Locate and identify every blood parasite.
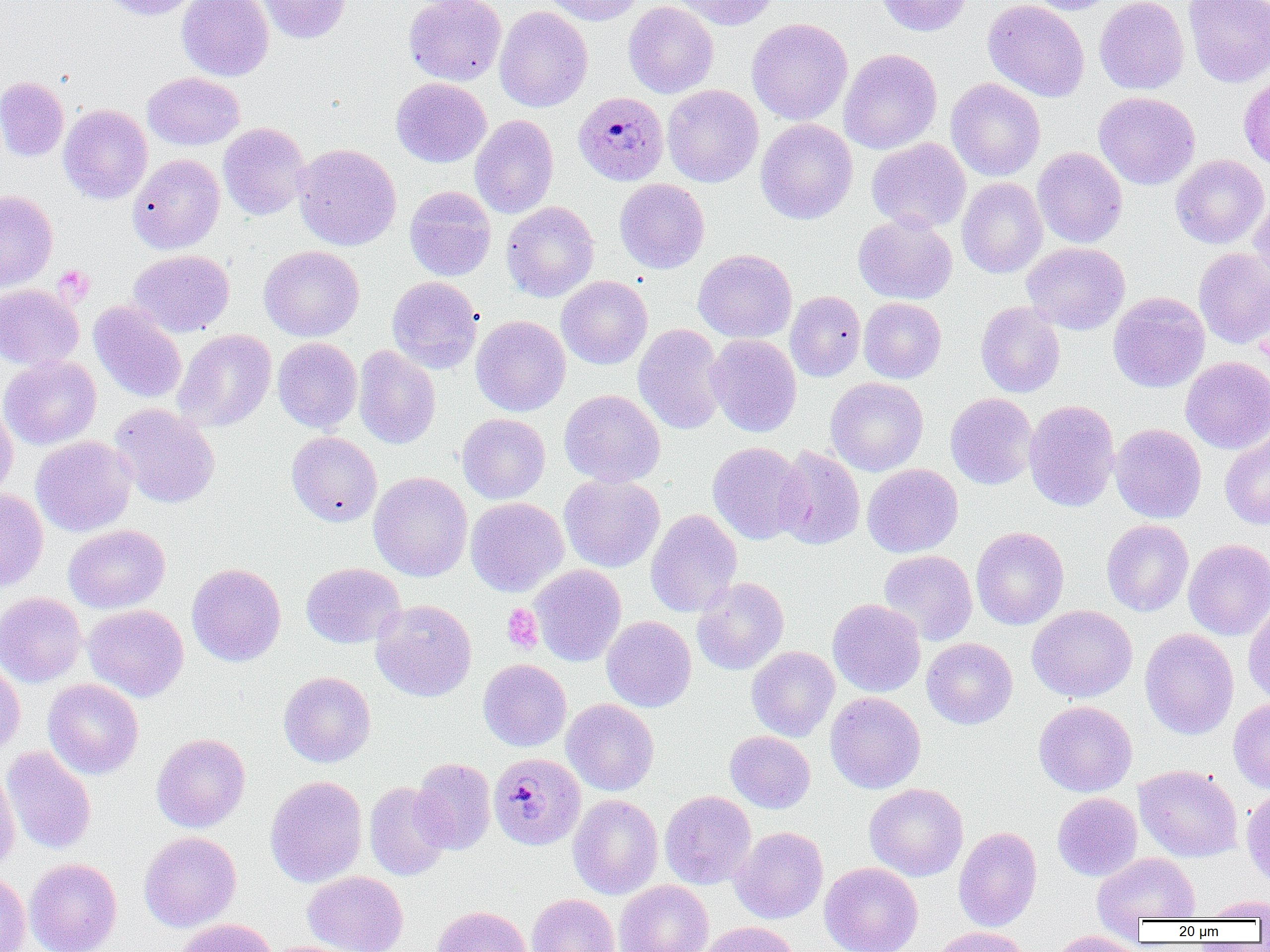

Approximate bounding boxes as named x1/y1/x2/y2 corners in pixels.
Plasmodium malariae-infected red blood cells: (x1=573, y1=91, x2=669, y2=185), (x1=488, y1=753, x2=585, y2=851).
No Plasmodium falciparum, Plasmodium ovale, Plasmodium vivax, Babesia divergens, or Trypanosoma brucei observed.

Summary:
  - Uninfected red blood cell locations: (x1=100, y1=0, x2=201, y2=20), (x1=177, y1=0, x2=274, y2=81), (x1=255, y1=0, x2=350, y2=43), (x1=404, y1=0, x2=506, y2=85), (x1=543, y1=0, x2=644, y2=26), (x1=671, y1=0, x2=780, y2=30), (x1=874, y1=0, x2=972, y2=37), (x1=982, y1=0, x2=1090, y2=101), (x1=1024, y1=0, x2=1120, y2=15), (x1=1094, y1=0, x2=1189, y2=94), (x1=623, y1=1, x2=718, y2=99), (x1=1183, y1=1, x2=1270, y2=88), (x1=494, y1=6, x2=593, y2=112), (x1=747, y1=18, x2=853, y2=125), (x1=839, y1=48, x2=942, y2=155), (x1=143, y1=72, x2=245, y2=150), (x1=1238, y1=75, x2=1270, y2=174), (x1=0, y1=76, x2=69, y2=161), (x1=391, y1=77, x2=491, y2=167), (x1=945, y1=78, x2=1045, y2=181), (x1=662, y1=84, x2=763, y2=187), (x1=1093, y1=92, x2=1200, y2=189), (x1=58, y1=104, x2=152, y2=204), (x1=470, y1=115, x2=558, y2=219), (x1=756, y1=119, x2=858, y2=224), (x1=218, y1=123, x2=311, y2=220), (x1=867, y1=137, x2=971, y2=233), (x1=293, y1=143, x2=401, y2=251), (x1=1032, y1=147, x2=1127, y2=248), (x1=128, y1=154, x2=224, y2=254), (x1=1170, y1=154, x2=1269, y2=249), (x1=957, y1=177, x2=1048, y2=278), (x1=615, y1=179, x2=709, y2=273), (x1=404, y1=186, x2=496, y2=281), (x1=0, y1=190, x2=58, y2=292), (x1=1249, y1=193, x2=1270, y2=290), (x1=501, y1=201, x2=599, y2=302), (x1=853, y1=213, x2=957, y2=304), (x1=1022, y1=242, x2=1130, y2=334), (x1=259, y1=245, x2=364, y2=342), (x1=1194, y1=248, x2=1270, y2=348), (x1=128, y1=249, x2=235, y2=337), (x1=693, y1=249, x2=796, y2=343), (x1=556, y1=275, x2=652, y2=369), (x1=387, y1=277, x2=482, y2=373), (x1=0, y1=285, x2=84, y2=369), (x1=785, y1=291, x2=866, y2=381), (x1=1108, y1=292, x2=1210, y2=392), (x1=858, y1=297, x2=947, y2=383), (x1=89, y1=302, x2=186, y2=403), (x1=976, y1=302, x2=1065, y2=398), (x1=471, y1=315, x2=570, y2=416), (x1=633, y1=324, x2=727, y2=434), (x1=173, y1=329, x2=276, y2=432), (x1=705, y1=334, x2=802, y2=437), (x1=273, y1=338, x2=362, y2=433), (x1=354, y1=345, x2=441, y2=449), (x1=0, y1=355, x2=101, y2=450), (x1=1181, y1=356, x2=1270, y2=453), (x1=825, y1=377, x2=928, y2=476), (x1=559, y1=389, x2=665, y2=487), (x1=945, y1=393, x2=1038, y2=489), (x1=1024, y1=399, x2=1120, y2=512), (x1=0, y1=401, x2=18, y2=500), (x1=109, y1=404, x2=220, y2=508), (x1=457, y1=413, x2=550, y2=503), (x1=1110, y1=423, x2=1206, y2=523), (x1=286, y1=431, x2=382, y2=527), (x1=1220, y1=431, x2=1270, y2=530), (x1=30, y1=435, x2=136, y2=537), (x1=707, y1=442, x2=807, y2=544), (x1=773, y1=446, x2=865, y2=550), (x1=862, y1=464, x2=963, y2=557), (x1=369, y1=471, x2=472, y2=581), (x1=559, y1=473, x2=665, y2=572), (x1=0, y1=489, x2=48, y2=592), (x1=465, y1=497, x2=568, y2=596), (x1=645, y1=509, x2=742, y2=618), (x1=1101, y1=519, x2=1193, y2=616), (x1=63, y1=524, x2=170, y2=613), (x1=971, y1=526, x2=1069, y2=630), (x1=1183, y1=538, x2=1270, y2=640), (x1=879, y1=550, x2=978, y2=646), (x1=300, y1=562, x2=405, y2=648), (x1=187, y1=563, x2=286, y2=666), (x1=529, y1=565, x2=627, y2=666), (x1=691, y1=577, x2=789, y2=675), (x1=0, y1=592, x2=87, y2=687), (x1=371, y1=599, x2=477, y2=702), (x1=827, y1=599, x2=926, y2=697), (x1=1242, y1=602, x2=1270, y2=706), (x1=83, y1=604, x2=188, y2=701), (x1=1026, y1=605, x2=1138, y2=702), (x1=601, y1=616, x2=696, y2=712), (x1=1140, y1=628, x2=1239, y2=740), (x1=921, y1=637, x2=1018, y2=729), (x1=747, y1=646, x2=840, y2=741), (x1=0, y1=658, x2=25, y2=758), (x1=478, y1=659, x2=571, y2=752), (x1=278, y1=671, x2=376, y2=767), (x1=43, y1=679, x2=143, y2=779), (x1=825, y1=692, x2=926, y2=794), (x1=1228, y1=697, x2=1270, y2=793), (x1=561, y1=699, x2=659, y2=796), (x1=1034, y1=700, x2=1137, y2=797), (x1=725, y1=730, x2=815, y2=813), (x1=151, y1=732, x2=250, y2=832), (x1=2, y1=746, x2=96, y2=855), (x1=411, y1=758, x2=496, y2=854), (x1=1134, y1=764, x2=1243, y2=862), (x1=0, y1=766, x2=20, y2=875), (x1=265, y1=776, x2=367, y2=887), (x1=364, y1=782, x2=452, y2=881), (x1=864, y1=783, x2=968, y2=882), (x1=1241, y1=788, x2=1270, y2=887), (x1=659, y1=791, x2=756, y2=889), (x1=1052, y1=792, x2=1142, y2=881), (x1=567, y1=795, x2=663, y2=899), (x1=730, y1=826, x2=829, y2=924), (x1=953, y1=827, x2=1042, y2=932), (x1=139, y1=831, x2=241, y2=932), (x1=1092, y1=852, x2=1201, y2=926), (x1=24, y1=858, x2=122, y2=952), (x1=819, y1=862, x2=923, y2=952), (x1=0, y1=870, x2=31, y2=952), (x1=302, y1=871, x2=408, y2=952), (x1=614, y1=880, x2=713, y2=952), (x1=527, y1=894, x2=620, y2=952), (x1=1201, y1=895, x2=1270, y2=920), (x1=431, y1=905, x2=533, y2=952), (x1=172, y1=919, x2=276, y2=952), (x1=695, y1=921, x2=799, y2=952), (x1=930, y1=927, x2=1033, y2=952), (x1=1048, y1=930, x2=1149, y2=952)
  - Platelet locations: (x1=54, y1=265, x2=94, y2=305), (x1=502, y1=604, x2=543, y2=653)
  - Slide-level diagnosis: Plasmodium malariae
  - Modality: light microscopy
  - Preparation: thin blood film
  - Field of view: single
  - Magnification: 1000x
  - Image size: 1270×952 pixels